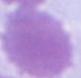

An erythrocyte is seen. Micrograph. Captured at 1000x magnification.